Give the preparation type.
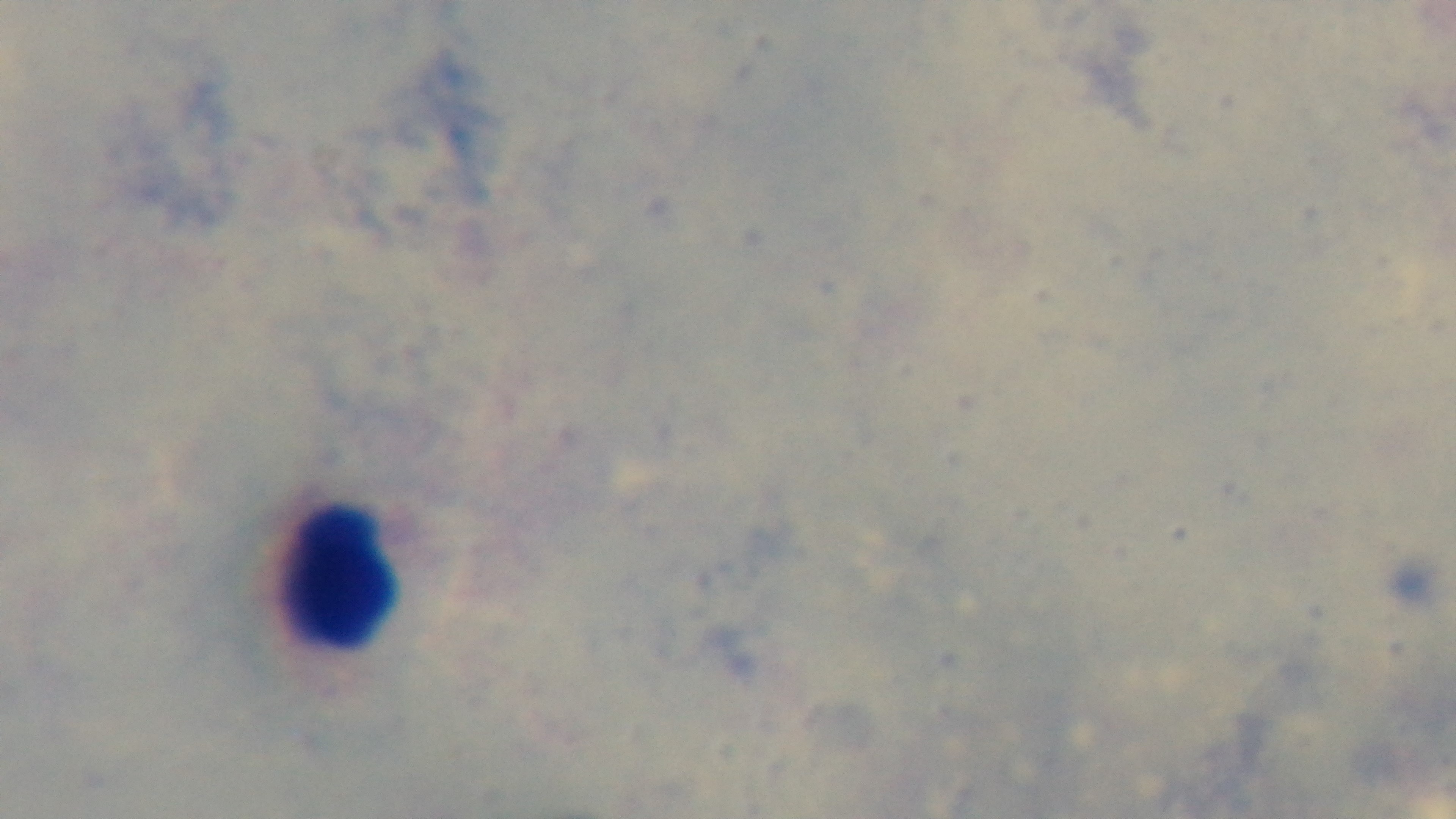
A thick smear.

Mounted 4K digital camera. Oil-immersion objective, 100x. Giemsa stain. Light microscopy. One field from the slide. Malaria status: negative.